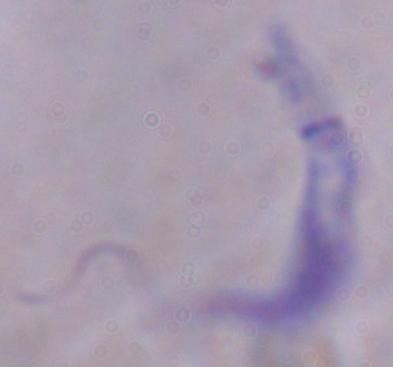

modality: micrograph
magnification: 1000x
identification: trypanosome